State which parasite is depicted.
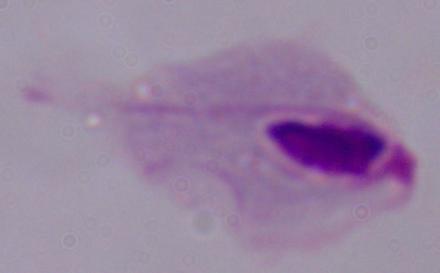

This is a trichomonad.

Summary:
  - Modality: photomicrograph
  - Magnification: 1000x